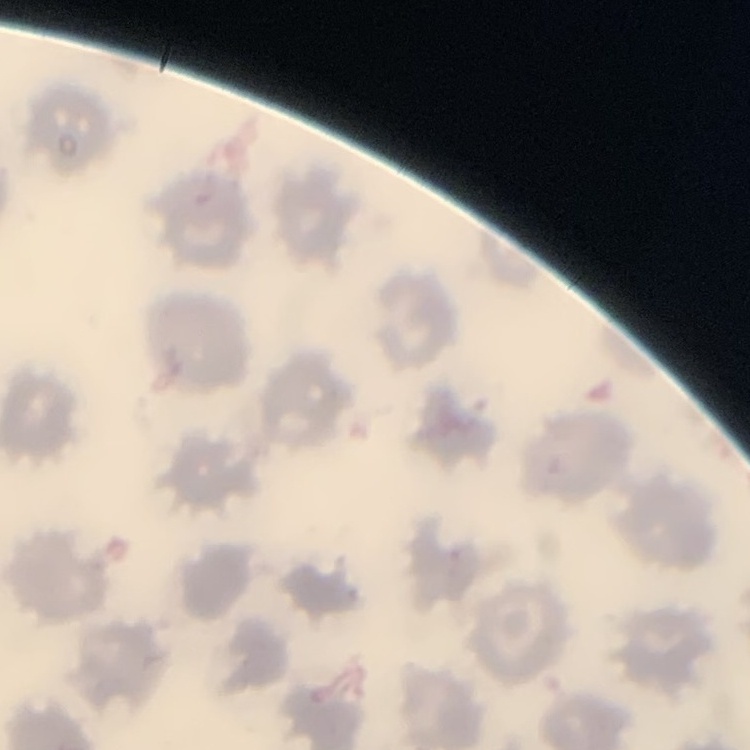
Summary:
  - Red blood cell morphology: no rouleaux formation
  - Stain: Field's or Giemsa
  - Image type: square crop of a larger photomicrograph
  - Preparation: thin blood film